Report the malaria status of this cell.
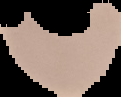

It is uninfected.

Summary:
  - Image size: 121×97 pixels
  - Preparation: thin blood film
  - Image type: segmented cell region on a black background